Report the malaria status of this cell.
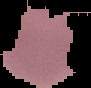
Parasitized.

{
  "preparation": "thin blood smear",
  "image_size": "91×88 pixels",
  "image_type": "segmented cell region on a black background"
}